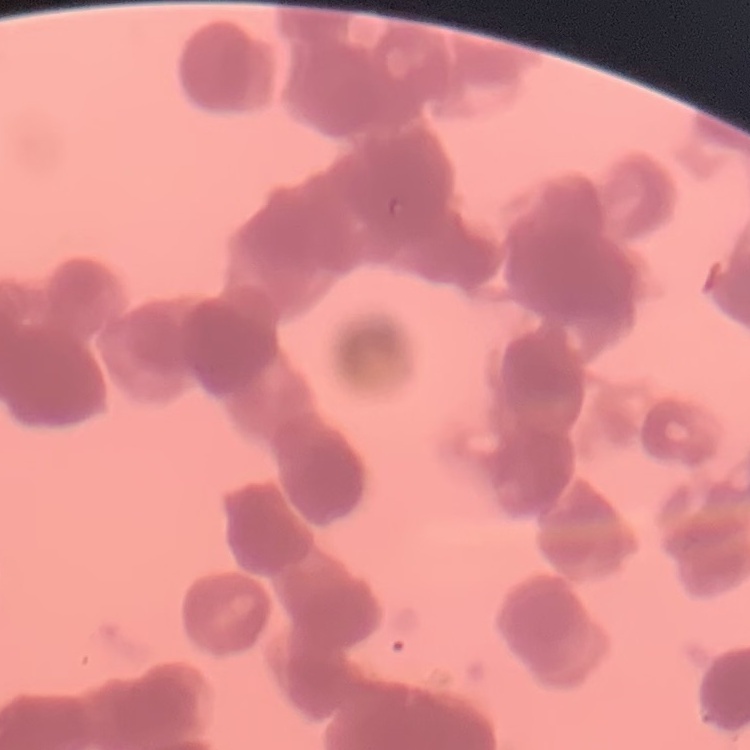

The red blood cells exhibit rouleaux formation. Square crop of a larger photomicrograph. Field's or Giemsa stain. Thin blood smear.